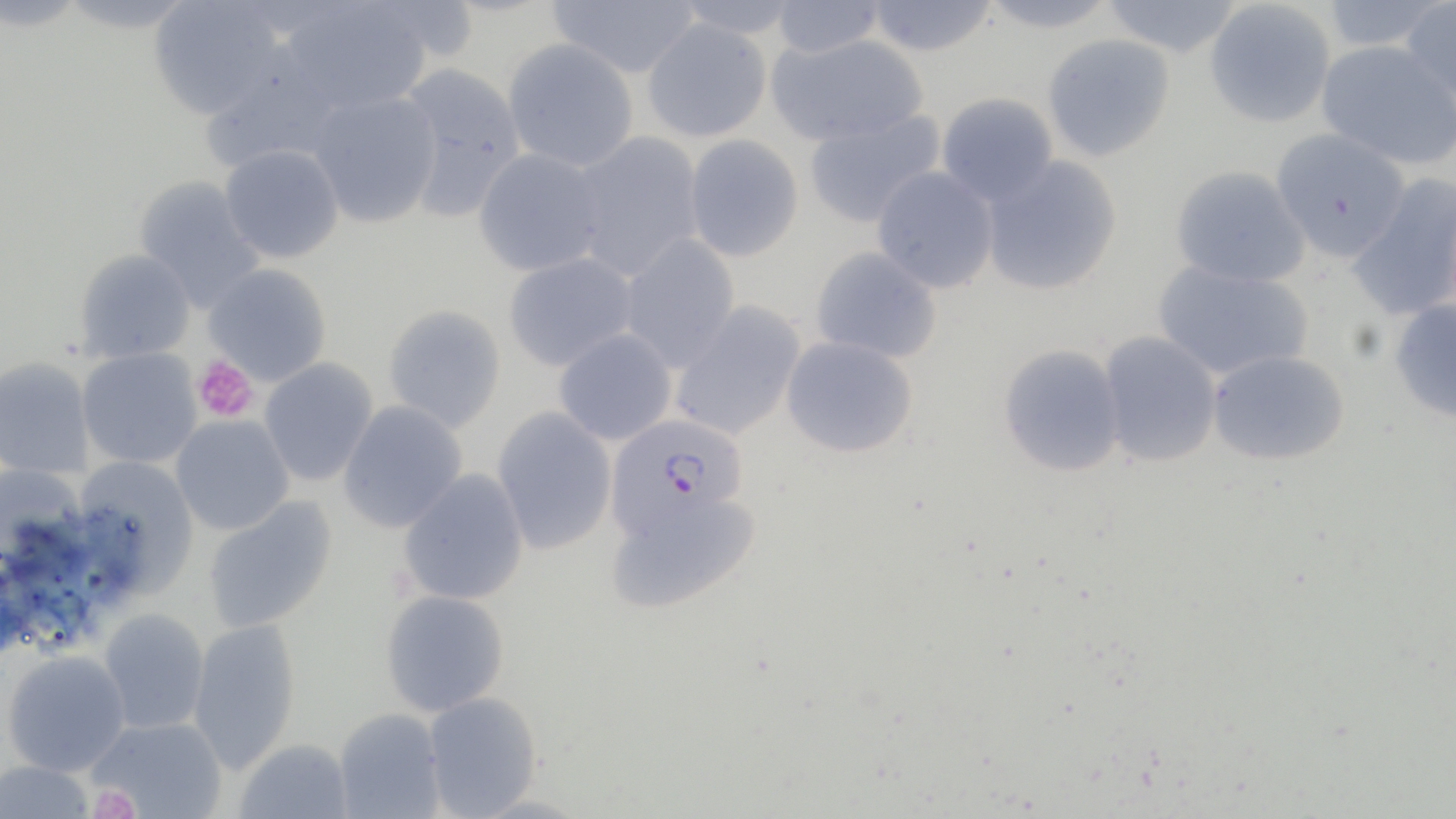
Summary:
  - Coordinate format: approximate bounding boxes as [x1, y1, x2, y2] in pixels
  - Plasmodium falciparum-infected red blood cell locations: [606, 413, 749, 536]
  - Uninfected red blood cell locations: [148, 0, 286, 120], [547, 0, 700, 79], [672, 0, 806, 39], [863, 0, 999, 57], [975, 0, 1123, 34], [1099, 0, 1244, 59], [1399, 0, 1456, 113], [279, 1, 433, 116], [769, 1, 884, 59], [1204, 1, 1336, 128], [1319, 1, 1448, 53], [641, 18, 773, 142], [767, 34, 928, 147], [1042, 34, 1175, 162], [501, 39, 639, 172], [1316, 40, 1455, 169], [394, 63, 526, 220], [306, 90, 442, 228], [936, 92, 1058, 206], [803, 109, 945, 228], [1270, 129, 1411, 261], [570, 132, 705, 282], [683, 134, 804, 263], [219, 144, 344, 264], [473, 148, 607, 277], [979, 154, 1123, 297], [1170, 165, 1310, 288], [871, 167, 999, 294], [1346, 175, 1456, 323], [133, 176, 265, 314], [618, 235, 740, 371], [810, 246, 942, 363], [74, 249, 196, 364], [503, 252, 637, 372], [1152, 261, 1314, 381], [203, 263, 332, 386], [1388, 299, 1456, 425], [669, 301, 806, 440], [383, 304, 506, 433], [553, 328, 677, 446], [1098, 331, 1223, 468], [781, 336, 918, 458], [998, 343, 1126, 477], [77, 348, 202, 469], [1207, 349, 1351, 467], [0, 357, 94, 479], [259, 358, 378, 487], [338, 401, 468, 533], [492, 406, 617, 555], [170, 415, 294, 535], [71, 456, 200, 600], [0, 463, 86, 566], [398, 469, 529, 606], [606, 488, 762, 615], [202, 496, 337, 633], [380, 589, 510, 717], [98, 609, 209, 734], [187, 618, 301, 773], [2, 650, 131, 776], [422, 692, 543, 817], [333, 708, 446, 819], [88, 717, 228, 818], [233, 738, 353, 819], [0, 760, 95, 818]
  - Platelet locations: [192, 355, 259, 423], [89, 786, 140, 819]
  - Slide-level diagnosis: Plasmodium falciparum
  - Image size: 1456×819 pixels
  - Stain: May-Grünwald-Giemsa
  - Modality: optical microscopy
  - Magnification: 1000x
  - Preparation: thin blood film
  - Field of view: single